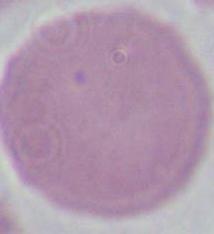
Summary:
  - Magnification: 1000x
  - Identification: red blood cell
  - Modality: photomicrograph